Describe the morphology of the red blood cells.
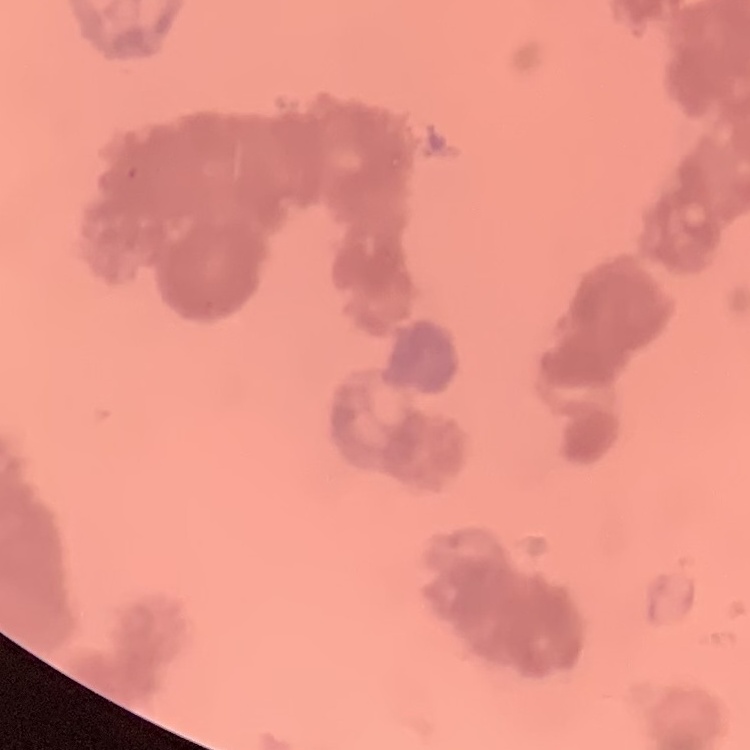
Rouleaux formation.

stain: Field's or Giemsa
preparation: thin blood smear
image_type: one tile cut from a larger photomicrograph